Describe the morphology of the erythrocytes.
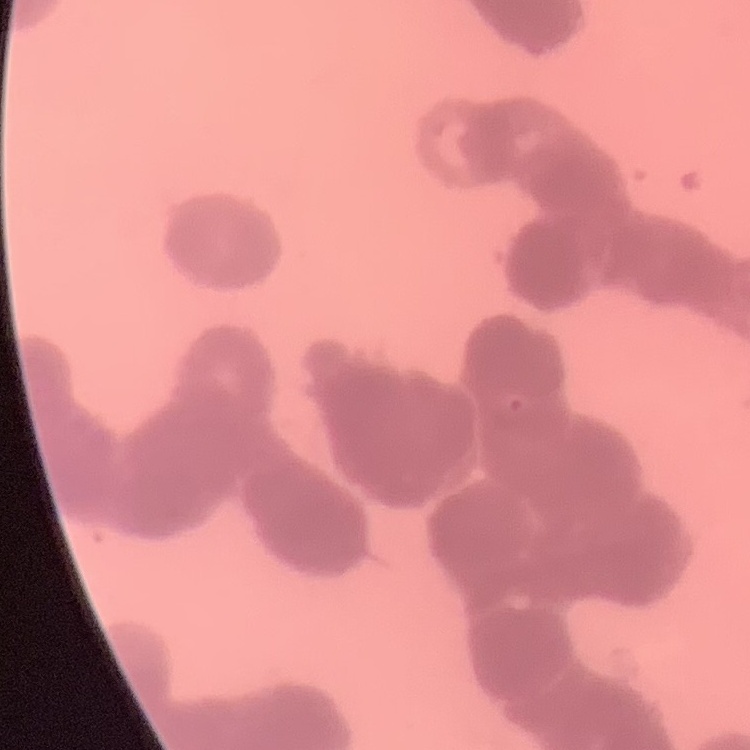

They show rouleaux formation.

image type = one tile cut from a larger photomicrograph
stain = Field's or Giemsa
preparation = thin peripheral smear